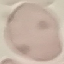 Result: no malaria parasites seen. Thin blood smear. Cell patch, automatically extracted from a larger field of view and resized to 64 × 64 pixels. Giemsa stain. Acquired by smartphone through the microscope eyepiece.